Give the position of every malaria parasite.
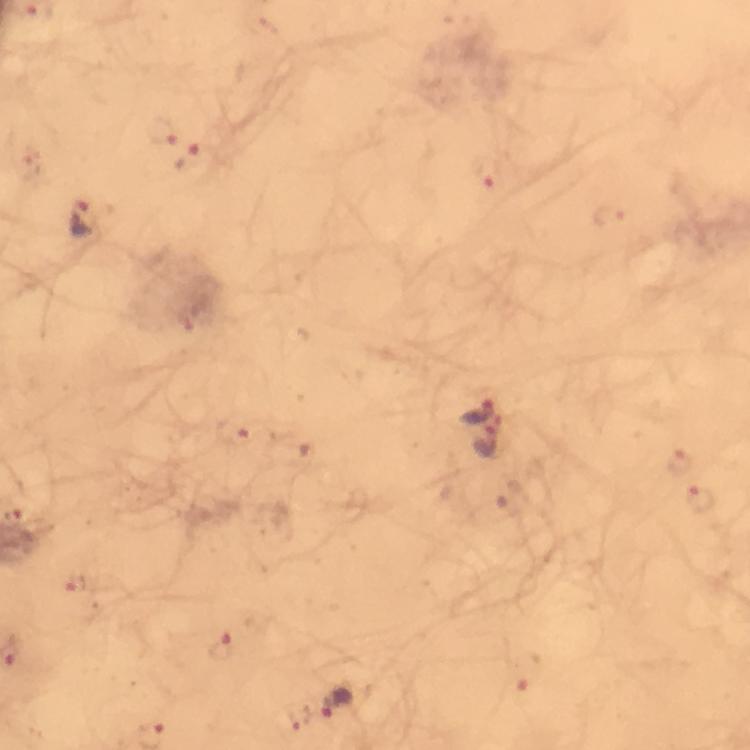

Approximate object centers, in pixels from the top-left corner.
Malaria parasites: (x=163, y=128), (x=189, y=159), (x=488, y=173), (x=609, y=217), (x=83, y=220), (x=479, y=410), (x=235, y=430), (x=487, y=441), (x=679, y=459), (x=699, y=497), (x=224, y=646), (x=339, y=702), (x=301, y=717).

Summary:
  - Preparation: thick blood smear
  - Cropped from: a single field of view
  - Image size: 750×750 pixels
  - Context: from a diagnostic examination for malaria
  - Capture: smartphone camera through the microscope
  - Magnification: 100x
  - Immersion oil: applied
  - Stain: Giemsa